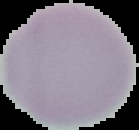

result = no malaria parasites detected
preparation = thin blood smear
image type = segmented cell region on a black background
image size = 139×130 pixels